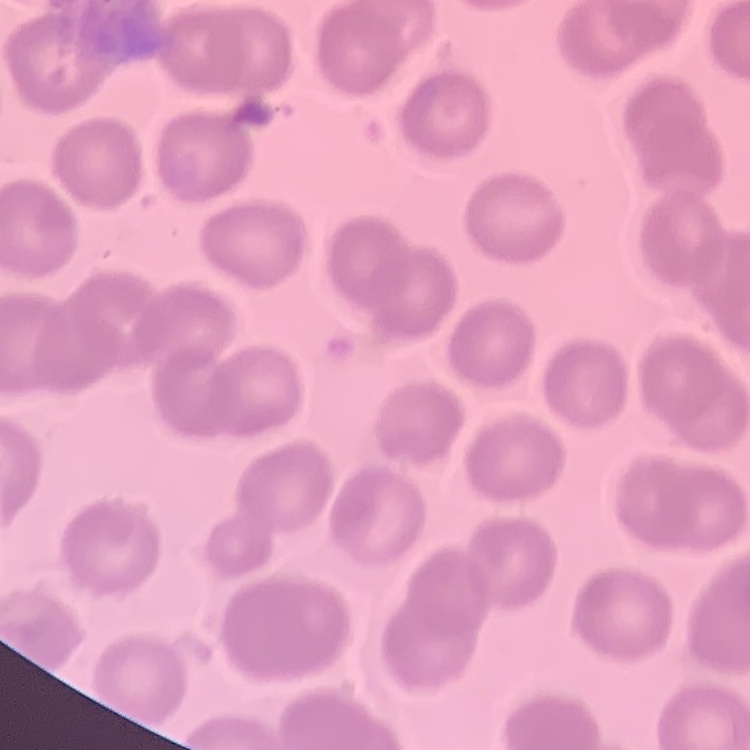
erythrocyte_morphology: no rouleaux formation
stain: Field's or Giemsa
preparation: thin peripheral smear
image_type: square crop of a larger photomicrograph